Classify this cell by malaria status.
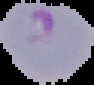

It is parasitized.

Summary:
  - Image size: 94×85 pixels
  - Image type: cell region segmented out of the field of view; surrounding area masked to black
  - Preparation: thin blood film